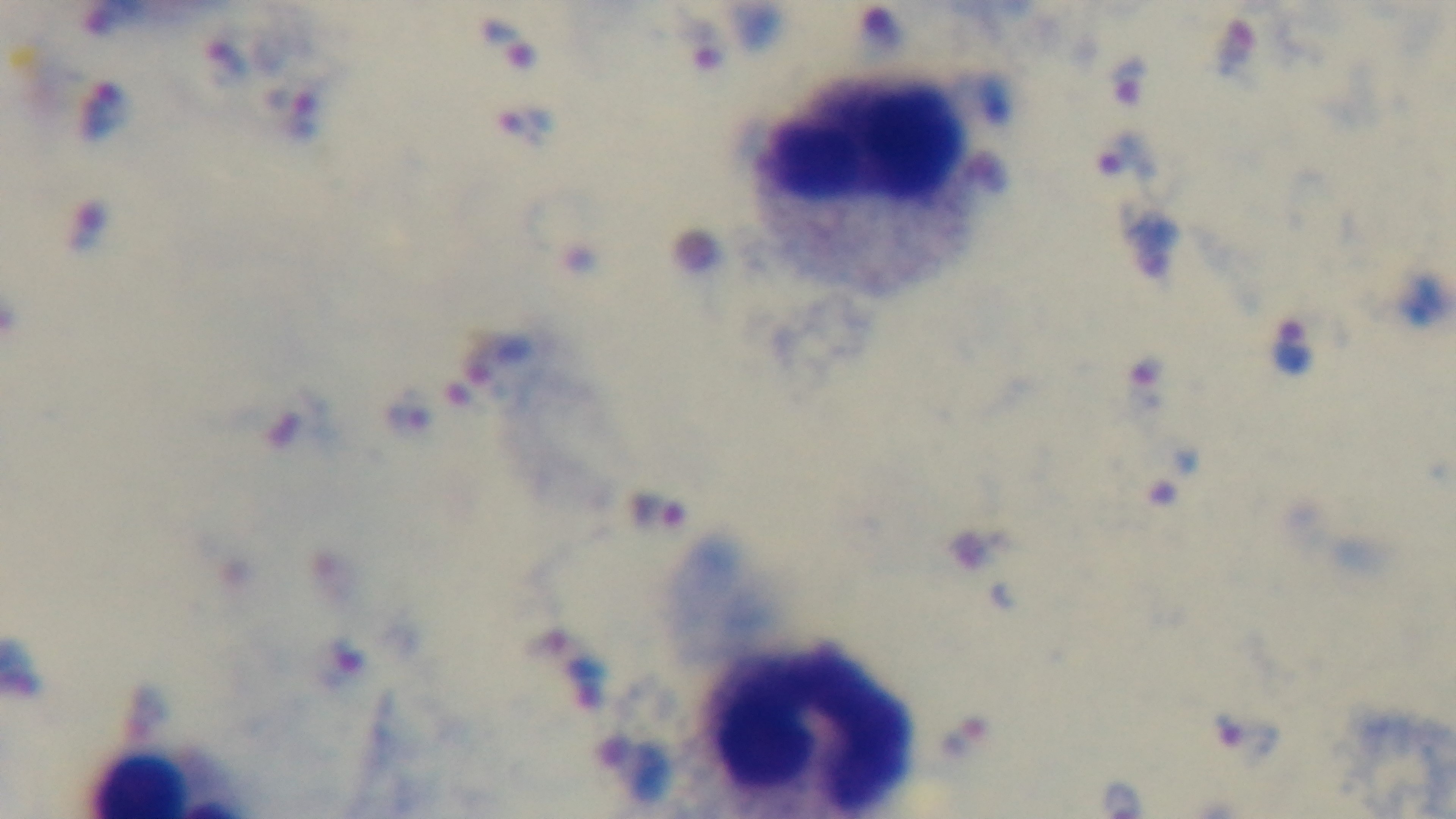
malaria status = positive
field of view = one from the slide
preparation = thick
objective = 100x oil immersion
stain = Giemsa
capture = mounted 4K digital camera
modality = light microscopy